State which cell type is depicted.
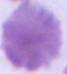

This is an erythrocyte.

{
  "magnification": "1000x",
  "modality": "photomicrograph"
}